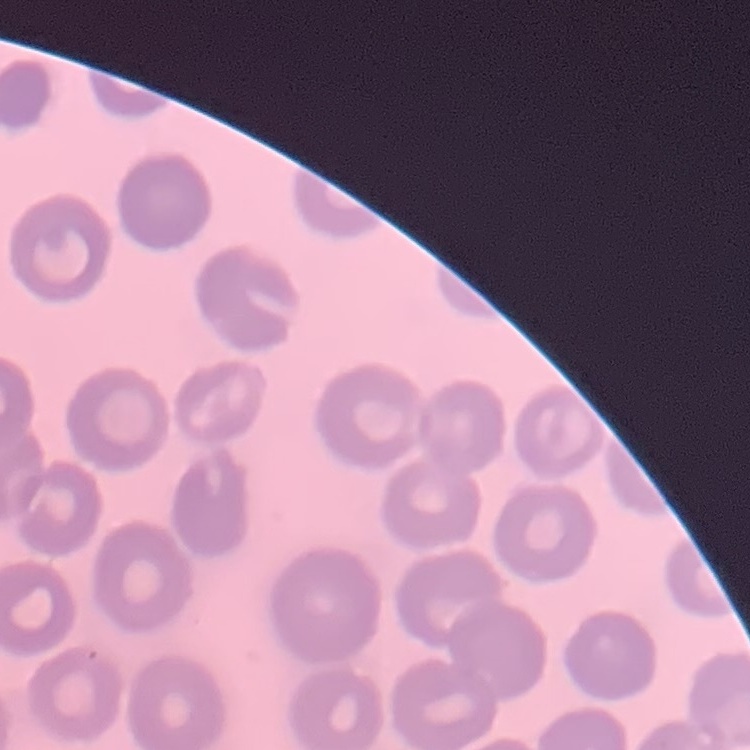
red blood cell morphology = no rouleaux formation
preparation = thin blood film
image type = square crop of a larger photomicrograph
stain = Field's or Giemsa